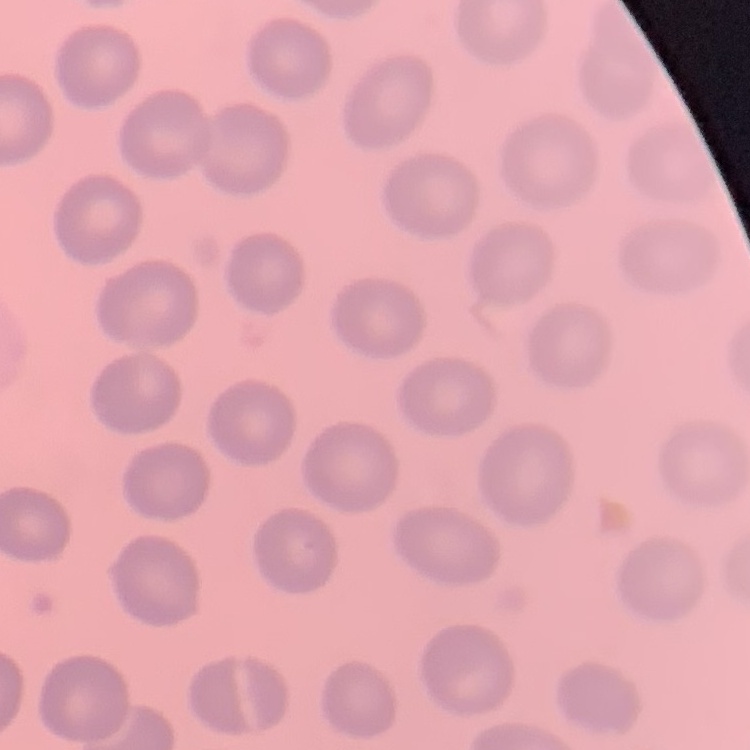
erythrocyte morphology = no rouleaux formation
preparation = thin peripheral smear
image type = one tile cut from a larger photomicrograph
stain = Field's or Giemsa